Report the malaria status of this cell.
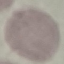

It is uninfected.

capture: smartphone camera at the microscope eyepiece
stain: Giemsa
preparation: thin smear
image_type: automatically extracted cell patch, resized to 64 × 64 pixels